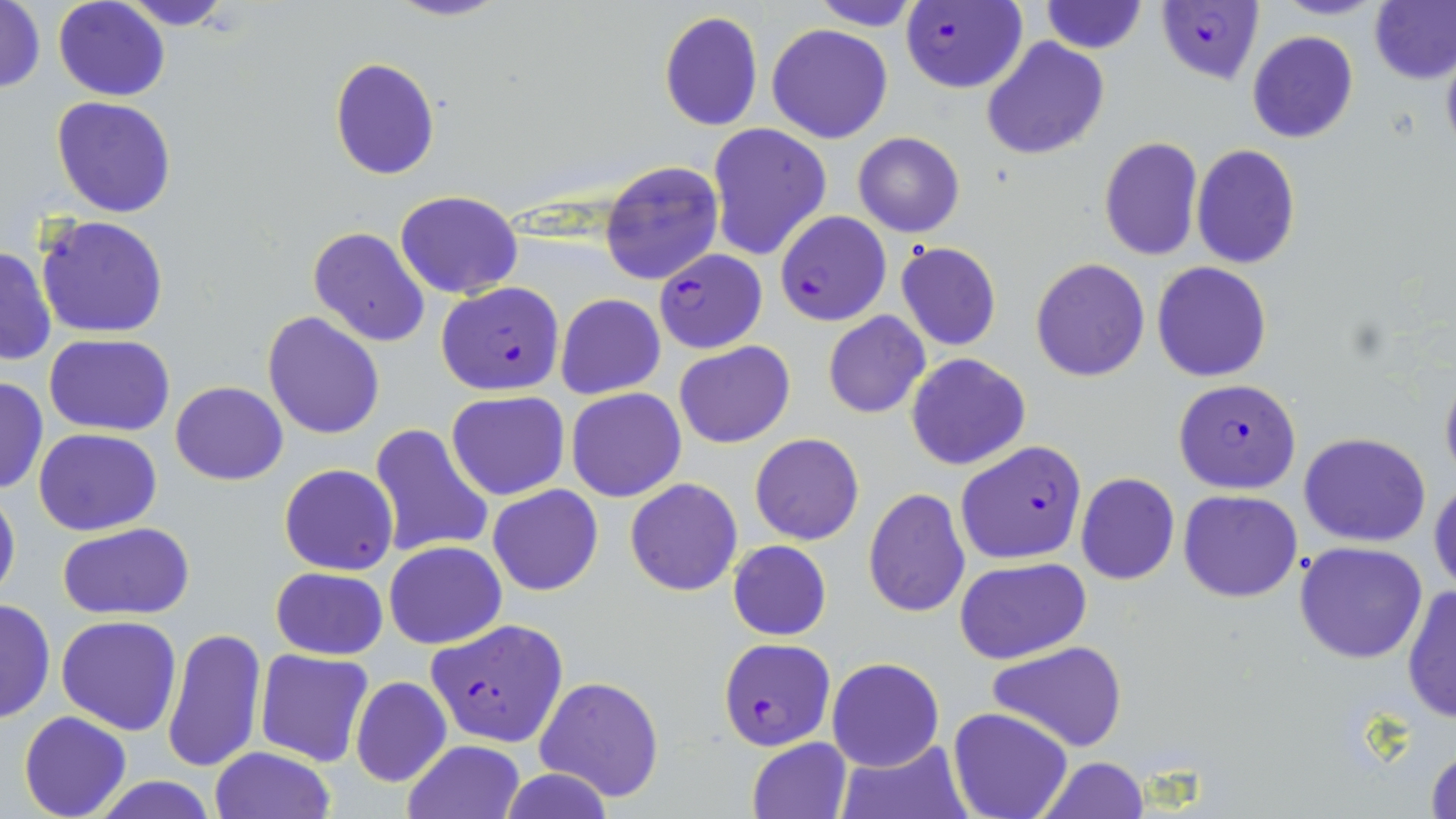

Approximate bounding boxes as (x1, y1, x2, y2) in pixels. Uninfected red blood cell locations: (111, 0, 238, 30), (384, 0, 510, 23), (807, 0, 925, 30), (1272, 0, 1383, 19), (1371, 0, 1456, 84), (53, 1, 170, 101), (1040, 1, 1147, 54), (1, 2, 46, 94), (658, 10, 764, 132), (767, 24, 894, 144), (1248, 31, 1359, 144), (981, 37, 1110, 159), (1439, 37, 1456, 162), (329, 57, 440, 180), (51, 97, 177, 219), (708, 125, 830, 261), (852, 132, 965, 237), (1098, 136, 1204, 260), (1191, 145, 1299, 267), (600, 161, 723, 285), (395, 191, 522, 299), (36, 215, 170, 338), (309, 226, 430, 348), (896, 242, 1002, 351), (1, 246, 55, 367), (1030, 258, 1150, 382), (1151, 262, 1273, 383), (556, 293, 666, 399), (823, 310, 930, 418), (262, 311, 385, 441), (45, 334, 177, 436), (674, 341, 795, 449), (905, 352, 1032, 470), (1439, 363, 1456, 488), (0, 376, 49, 495), (171, 382, 288, 484), (567, 388, 686, 502), (446, 391, 571, 500), (368, 424, 493, 560), (34, 428, 161, 534), (750, 431, 864, 545), (1300, 431, 1431, 547), (279, 464, 399, 575), (1076, 473, 1179, 585), (1430, 476, 1456, 592), (625, 478, 743, 596), (0, 481, 21, 607), (487, 484, 603, 596), (863, 488, 971, 616), (1178, 490, 1303, 603), (59, 522, 194, 621), (384, 540, 507, 649), (727, 541, 832, 640), (1295, 542, 1427, 664), (953, 557, 1091, 664), (271, 566, 388, 660), (1402, 584, 1456, 724), (0, 596, 55, 724), (56, 615, 182, 736), (162, 626, 267, 773), (988, 641, 1128, 752), (255, 648, 373, 766), (826, 657, 944, 771), (534, 674, 665, 804), (350, 676, 452, 787), (948, 707, 1074, 819), (18, 711, 131, 819), (745, 737, 852, 819), (833, 738, 972, 819), (403, 740, 524, 818), (1424, 744, 1455, 819), (210, 747, 335, 819), (1036, 756, 1150, 819), (501, 770, 615, 819), (88, 776, 223, 818). Plasmodium falciparum-infected red blood cell locations: (1156, 1, 1263, 85), (900, 2, 1028, 93), (775, 211, 891, 326), (654, 249, 767, 353), (436, 282, 566, 395), (1173, 378, 1301, 494), (955, 440, 1087, 564), (426, 618, 571, 748), (720, 637, 833, 749). Slide-level diagnosis: Plasmodium falciparum. May-Grünwald-Giemsa-stained preparation. 1000x magnification. Optical microscopy. Thin blood smear. Single field of view. Image is 1456×819 pixels.